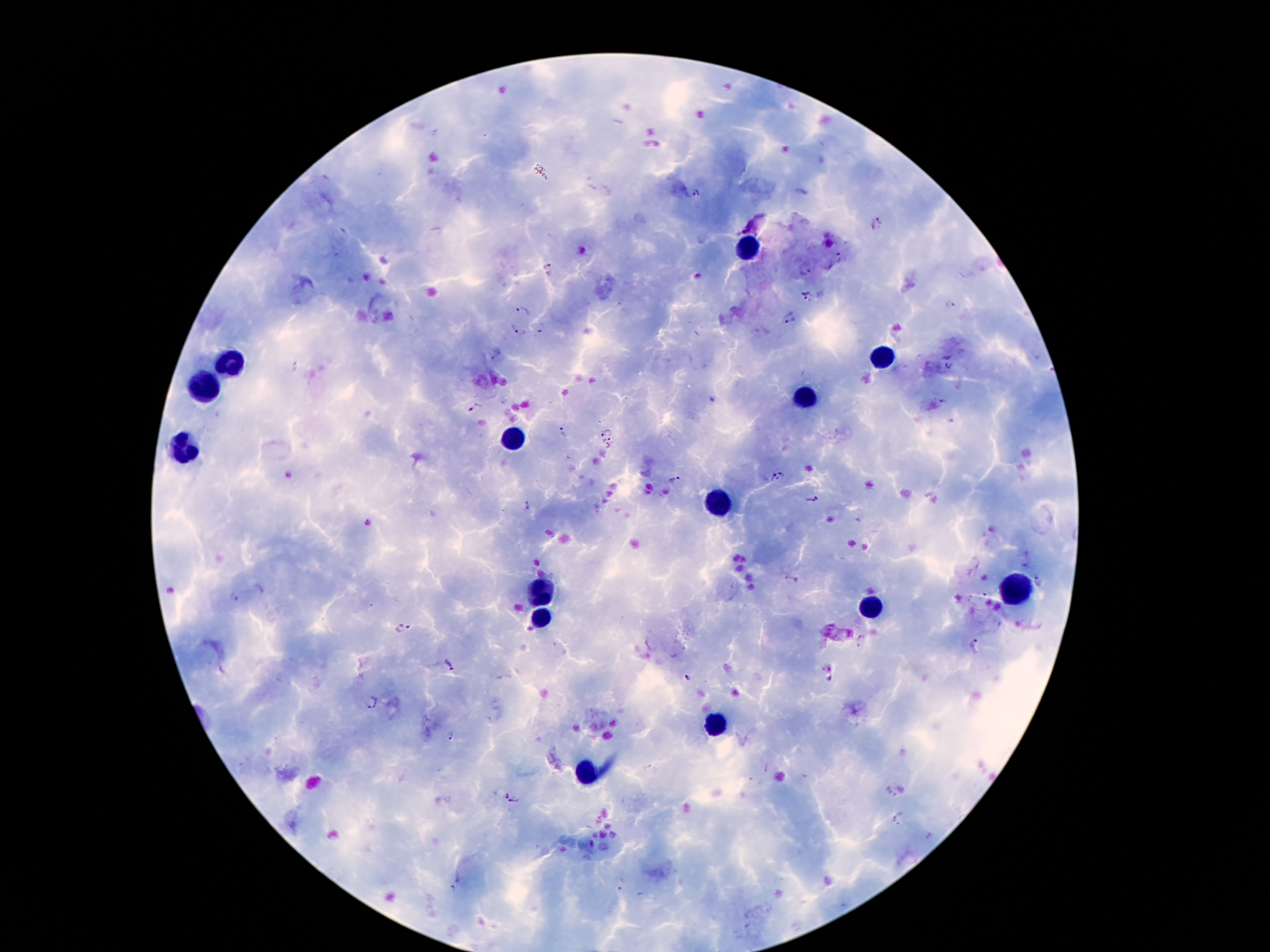
coordinate format = approximate centers as [x, y] in pixels
malaria parasite locations = [696, 193], [877, 221], [840, 258], [548, 269], [805, 270], [808, 297], [950, 305], [523, 311], [789, 319], [540, 329], [518, 331], [950, 366], [945, 402], [476, 409], [606, 431], [562, 434], [607, 444], [776, 478], [676, 482], [811, 498], [529, 507], [234, 597], [401, 630], [975, 646], [449, 665], [824, 667], [688, 678], [372, 702], [450, 738], [889, 793], [511, 800], [898, 818]
leukocyte locations = [750, 251], [885, 358], [230, 365], [201, 387], [803, 396], [511, 441], [184, 450], [719, 502], [1014, 588], [535, 593], [868, 608], [537, 618], [715, 729], [587, 774]
patient malaria status = positive for Plasmodium falciparum
stain = Giemsa
image size = 1270×952 pixels
field of view = one from this slide
preparation = thick blood film
capture = smartphone through the microscope eyepiece
magnification = 100x